Locate every Plasmodium falciparum-infected red blood cell.
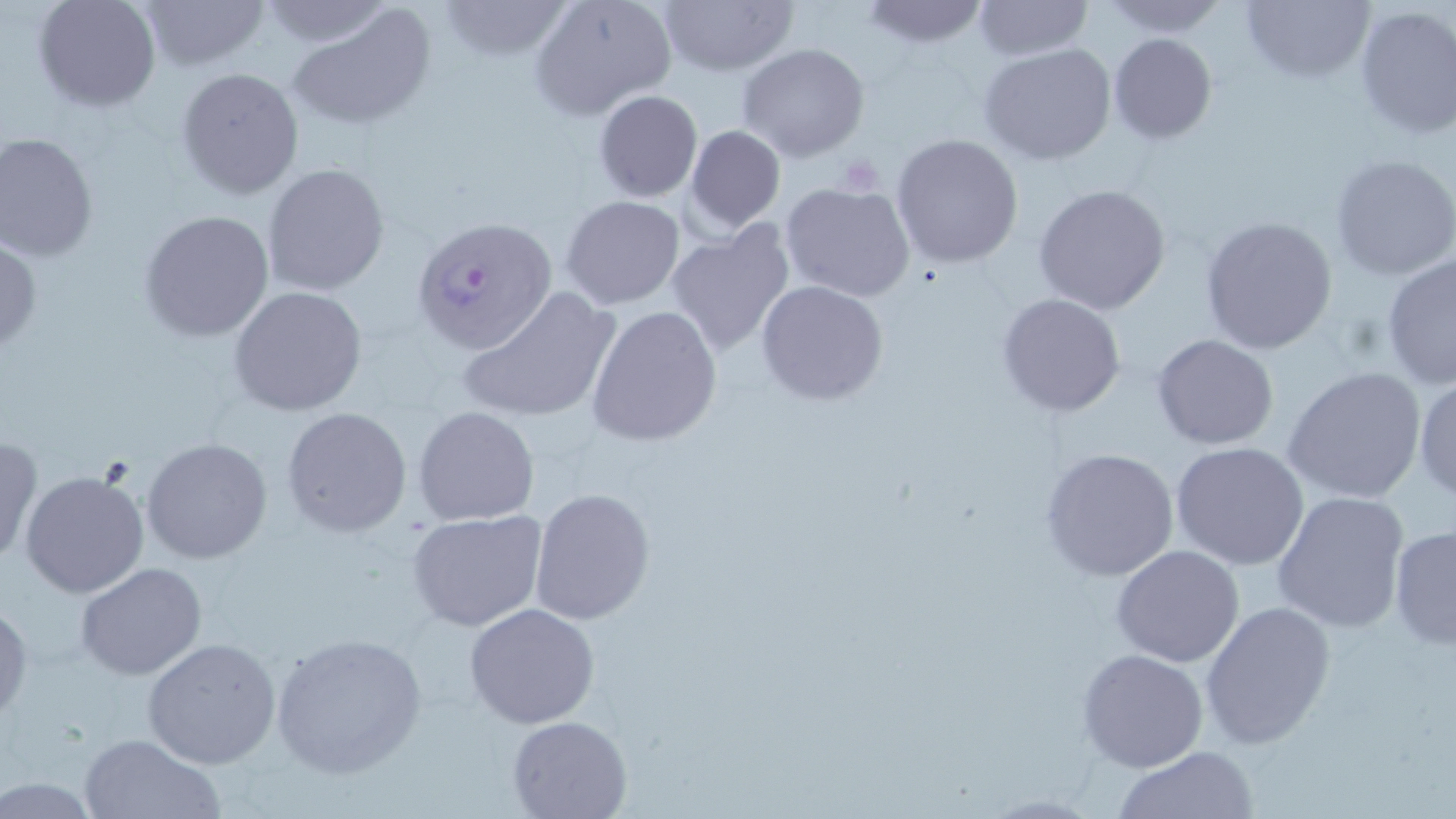

Approximate bounding boxes as (x1,y1)-(x2,y2) corner pairs in pixels.
Plasmodium falciparum-infected red blood cells: (412,214)-(557,353).

Uninfected red blood cell locations: (33,0)-(160,112), (137,0)-(269,72), (435,0)-(575,62), (529,0)-(677,120), (658,0)-(799,74), (858,0)-(991,48), (971,0)-(1091,62), (1241,0)-(1375,85), (1098,1)-(1229,38), (1353,3)-(1456,139), (286,5)-(439,131), (1108,33)-(1217,145), (737,43)-(870,162), (978,43)-(1119,167), (177,68)-(303,199), (593,89)-(702,202), (684,124)-(786,233), (0,132)-(99,261), (891,132)-(1024,268), (1329,152)-(1456,281), (261,162)-(391,296), (248,167)-(381,418), (781,180)-(916,301), (1032,184)-(1172,316), (560,195)-(686,310), (140,210)-(273,341), (1199,216)-(1339,356), (665,220)-(796,358), (0,235)-(41,354), (1381,254)-(1456,390), (756,280)-(889,405), (228,286)-(368,415), (457,286)-(621,426), (996,292)-(1127,419), (585,306)-(723,446), (1151,334)-(1280,451), (1281,365)-(1428,506), (1412,371)-(1456,502), (413,406)-(540,527), (282,407)-(413,538), (1,433)-(41,566), (141,438)-(273,564), (1170,441)-(1311,572), (1039,447)-(1180,581), (21,468)-(150,597), (529,488)-(657,626), (1271,490)-(1408,633), (406,510)-(548,632), (1389,524)-(1456,651), (1111,544)-(1244,666), (75,564)-(206,681), (0,597)-(32,725), (1199,600)-(1335,749), (464,602)-(599,729), (268,631)-(428,780), (140,638)-(282,770), (1078,648)-(1208,773), (507,714)-(631,818), (77,732)-(225,819), (1114,745)-(1260,818). Platelet locations: (834,157)-(883,197). Slide-level diagnosis: Plasmodium falciparum. 1000x magnification. Thin blood film. Image is 1456×819 pixels. One field of a larger specimen. Optical microscopy. May-Grünwald-Giemsa-stained preparation.